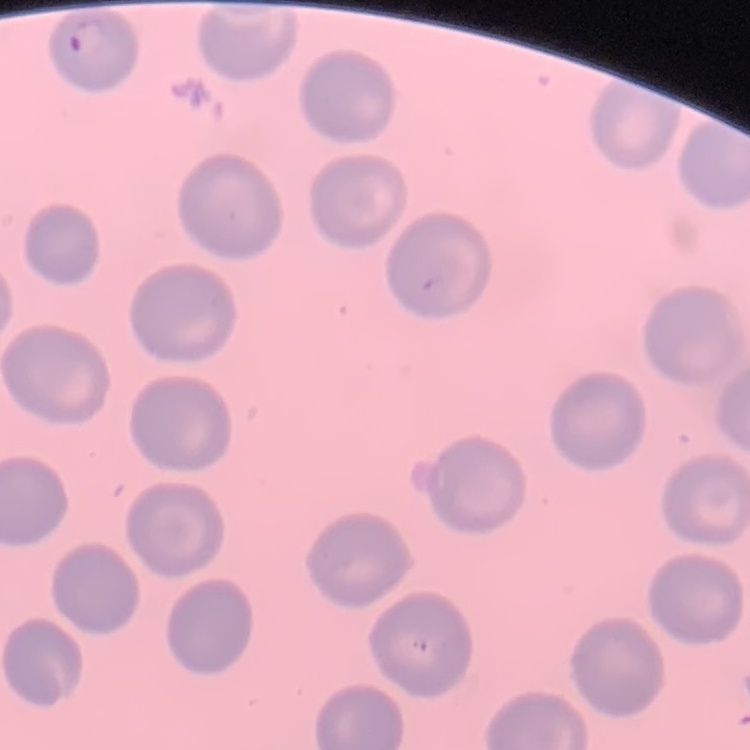
erythrocyte_morphology: no rouleaux formation
preparation: thin blood film
image_type: square crop of a larger photomicrograph
stain: Field's or Giemsa